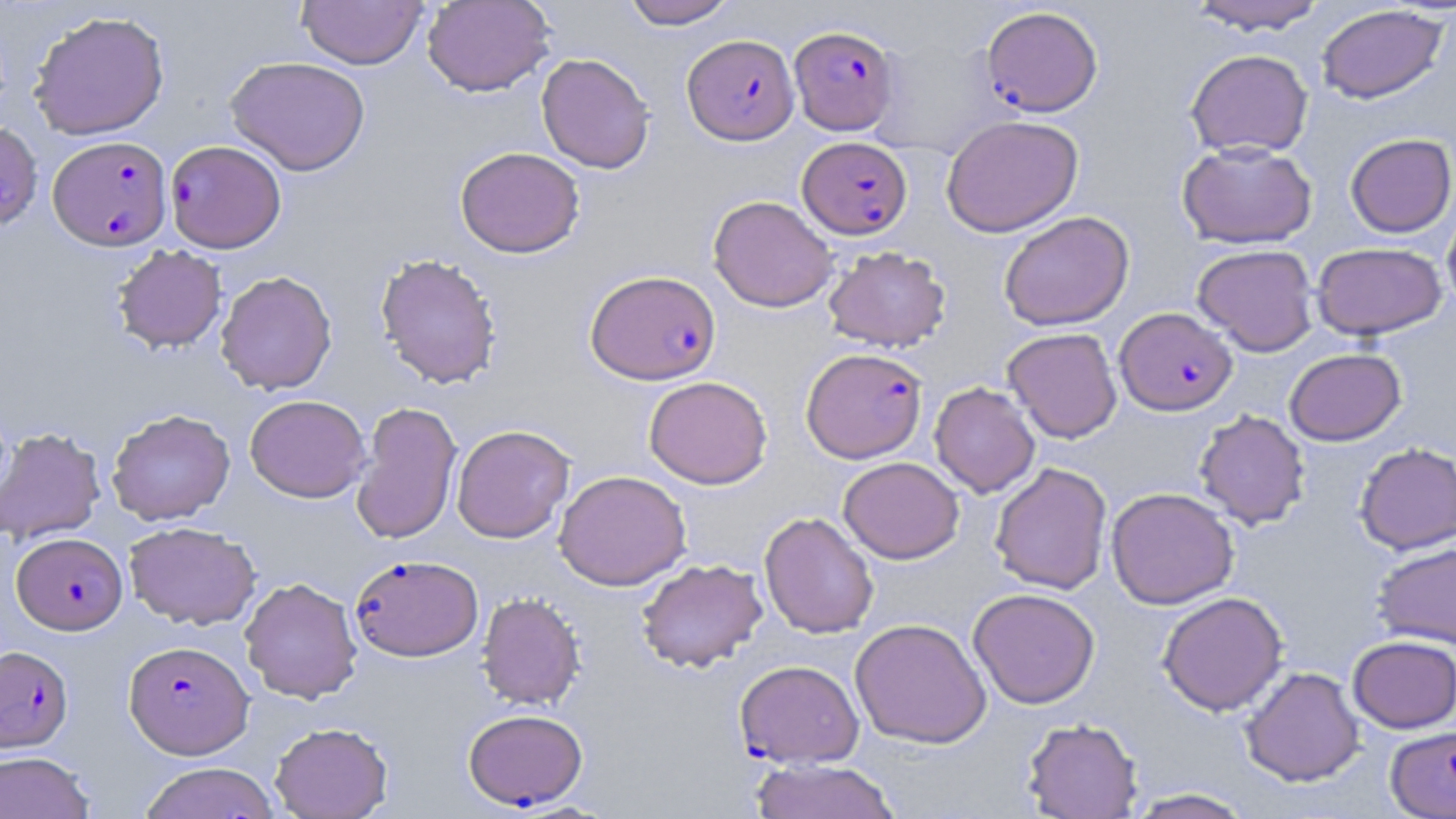
slide-level diagnosis = Plasmodium falciparum
modality = optical microscopy
stain = May-Grünwald-Giemsa
field of view = one of a larger specimen
magnification = 1000x
uninfected red blood cell locations = approximate bounding boxes as named x1/y1/x2/y2 corners in pixels: (x1=297, y1=0, x2=428, y2=69), (x1=422, y1=0, x2=555, y2=97), (x1=620, y1=0, x2=738, y2=28), (x1=1186, y1=0, x2=1330, y2=34), (x1=1316, y1=5, x2=1448, y2=104), (x1=29, y1=10, x2=170, y2=141), (x1=1185, y1=49, x2=1313, y2=159), (x1=536, y1=53, x2=655, y2=174), (x1=225, y1=55, x2=370, y2=175), (x1=942, y1=115, x2=1083, y2=237), (x1=0, y1=121, x2=43, y2=231), (x1=1345, y1=133, x2=1455, y2=237), (x1=1177, y1=141, x2=1318, y2=249), (x1=455, y1=146, x2=585, y2=258), (x1=708, y1=195, x2=838, y2=312), (x1=1441, y1=204, x2=1456, y2=316), (x1=998, y1=210, x2=1134, y2=331), (x1=1312, y1=242, x2=1448, y2=340), (x1=112, y1=244, x2=227, y2=353), (x1=1192, y1=244, x2=1319, y2=356), (x1=822, y1=245, x2=951, y2=353), (x1=374, y1=253, x2=502, y2=389), (x1=216, y1=270, x2=338, y2=395), (x1=1002, y1=327, x2=1122, y2=443), (x1=1284, y1=347, x2=1406, y2=445), (x1=644, y1=375, x2=773, y2=489), (x1=929, y1=382, x2=1040, y2=497), (x1=245, y1=394, x2=370, y2=502), (x1=351, y1=401, x2=462, y2=544), (x1=106, y1=408, x2=236, y2=525), (x1=1194, y1=409, x2=1311, y2=530), (x1=451, y1=424, x2=574, y2=543), (x1=0, y1=426, x2=106, y2=545), (x1=1354, y1=442, x2=1456, y2=554), (x1=838, y1=456, x2=964, y2=563), (x1=990, y1=462, x2=1112, y2=595), (x1=554, y1=469, x2=691, y2=590), (x1=1106, y1=487, x2=1239, y2=609), (x1=759, y1=512, x2=879, y2=639), (x1=124, y1=521, x2=261, y2=630), (x1=1372, y1=541, x2=1456, y2=650), (x1=636, y1=558, x2=768, y2=673), (x1=240, y1=576, x2=363, y2=703), (x1=968, y1=588, x2=1101, y2=709), (x1=476, y1=591, x2=585, y2=710), (x1=1158, y1=591, x2=1288, y2=716), (x1=850, y1=618, x2=991, y2=749), (x1=1347, y1=635, x2=1456, y2=733), (x1=1240, y1=666, x2=1365, y2=786), (x1=1021, y1=717, x2=1143, y2=818), (x1=270, y1=722, x2=393, y2=819), (x1=0, y1=751, x2=95, y2=819), (x1=749, y1=758, x2=902, y2=819), (x1=138, y1=762, x2=281, y2=819), (x1=1123, y1=788, x2=1256, y2=818)
image size = 1456×819 pixels
preparation = thin blood film
Plasmodium falciparum-infected red blood cell locations = approximate bounding boxes as named x1/y1/x2/y2 corners in pixels: (x1=981, y1=5, x2=1103, y2=117), (x1=790, y1=24, x2=899, y2=135), (x1=683, y1=33, x2=799, y2=144), (x1=48, y1=135, x2=172, y2=251), (x1=798, y1=136, x2=912, y2=239), (x1=163, y1=142, x2=284, y2=255), (x1=585, y1=269, x2=721, y2=384), (x1=1115, y1=307, x2=1237, y2=415), (x1=801, y1=347, x2=927, y2=463), (x1=11, y1=532, x2=127, y2=635), (x1=350, y1=554, x2=483, y2=661), (x1=124, y1=640, x2=254, y2=759), (x1=3, y1=649, x2=76, y2=755), (x1=736, y1=668, x2=865, y2=775), (x1=463, y1=708, x2=588, y2=811), (x1=1385, y1=725, x2=1456, y2=818)